Locate every uninfected red blood cell.
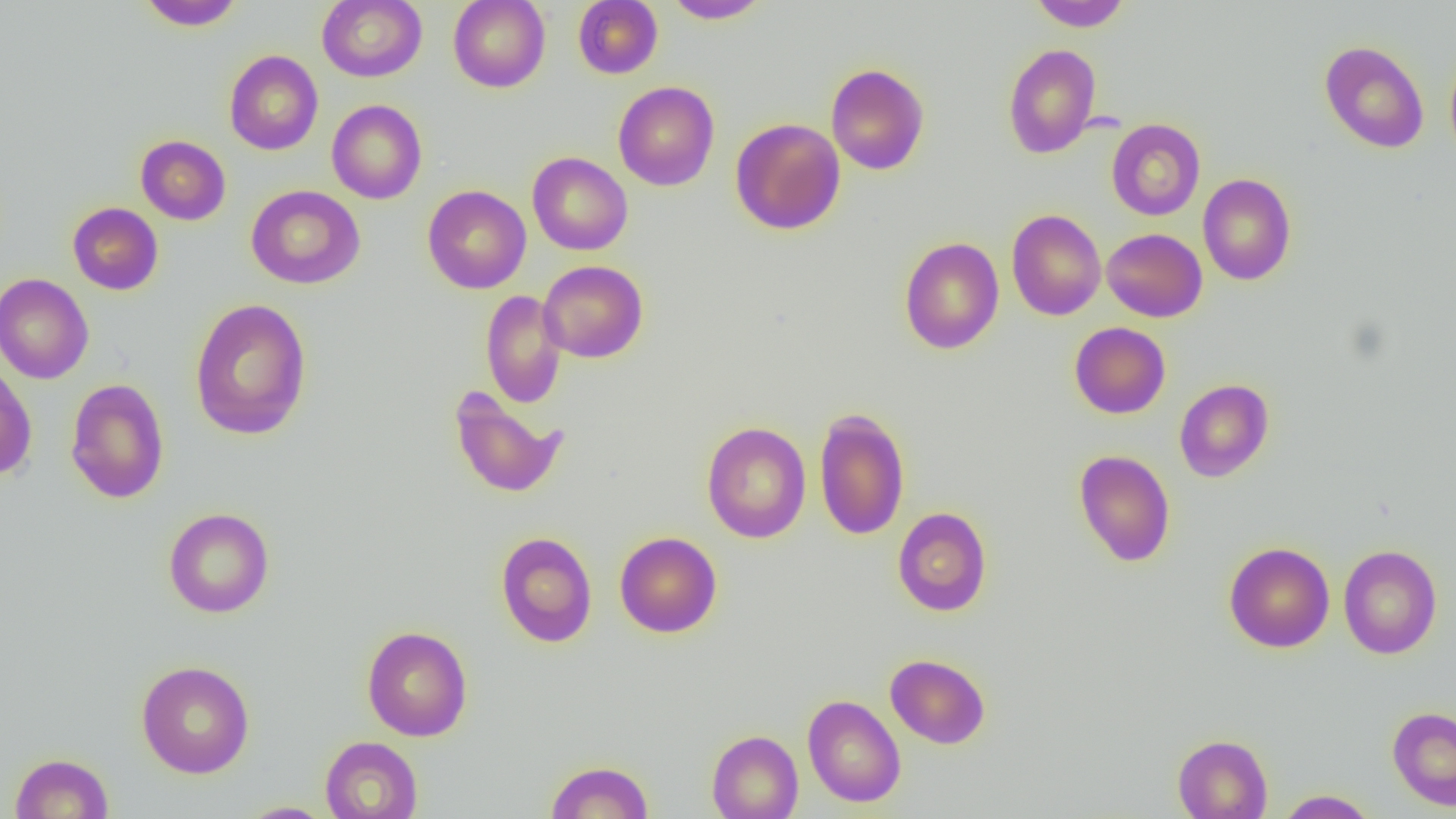

Approximate bounding boxes as [x1, y1, x2, y2] in pixels.
Uninfected red blood cells: [317, 0, 426, 82], [448, 0, 550, 92], [573, 0, 662, 79], [662, 0, 773, 24], [1027, 0, 1132, 31], [137, 1, 244, 30], [1319, 40, 1430, 153], [1003, 43, 1101, 159], [1444, 44, 1456, 169], [224, 50, 323, 155], [825, 63, 929, 175], [613, 81, 720, 191], [327, 99, 427, 204], [730, 118, 845, 235], [1106, 118, 1206, 220], [136, 135, 230, 225], [528, 152, 633, 255], [1198, 173, 1297, 285], [246, 185, 365, 289], [422, 185, 531, 293], [67, 202, 163, 295], [1006, 209, 1106, 320], [1102, 228, 1207, 322], [899, 237, 1004, 354], [538, 260, 648, 363], [0, 273, 94, 384], [480, 290, 567, 408], [189, 298, 312, 440], [1069, 322, 1170, 418], [0, 362, 37, 481], [65, 378, 169, 504], [1174, 378, 1274, 482], [449, 387, 567, 499], [814, 407, 910, 541], [701, 421, 811, 543], [1074, 449, 1175, 567], [892, 506, 992, 616], [163, 507, 275, 618], [614, 531, 722, 637], [495, 532, 597, 647], [1223, 541, 1335, 653], [1338, 545, 1442, 659], [361, 625, 473, 741], [885, 654, 990, 749], [136, 660, 255, 778], [803, 694, 906, 808], [1387, 707, 1456, 810], [706, 729, 804, 819], [1172, 734, 1272, 818], [320, 736, 422, 819], [10, 752, 114, 818], [544, 760, 655, 819], [1276, 789, 1379, 818], [236, 801, 338, 818].

slide_level_diagnosis: negative for blood parasites
image_size: 1456×819 pixels
modality: optical microscopy
field_of_view: one of a larger specimen
magnification: 1000x
preparation: thin blood film